Point out each leukocyte.
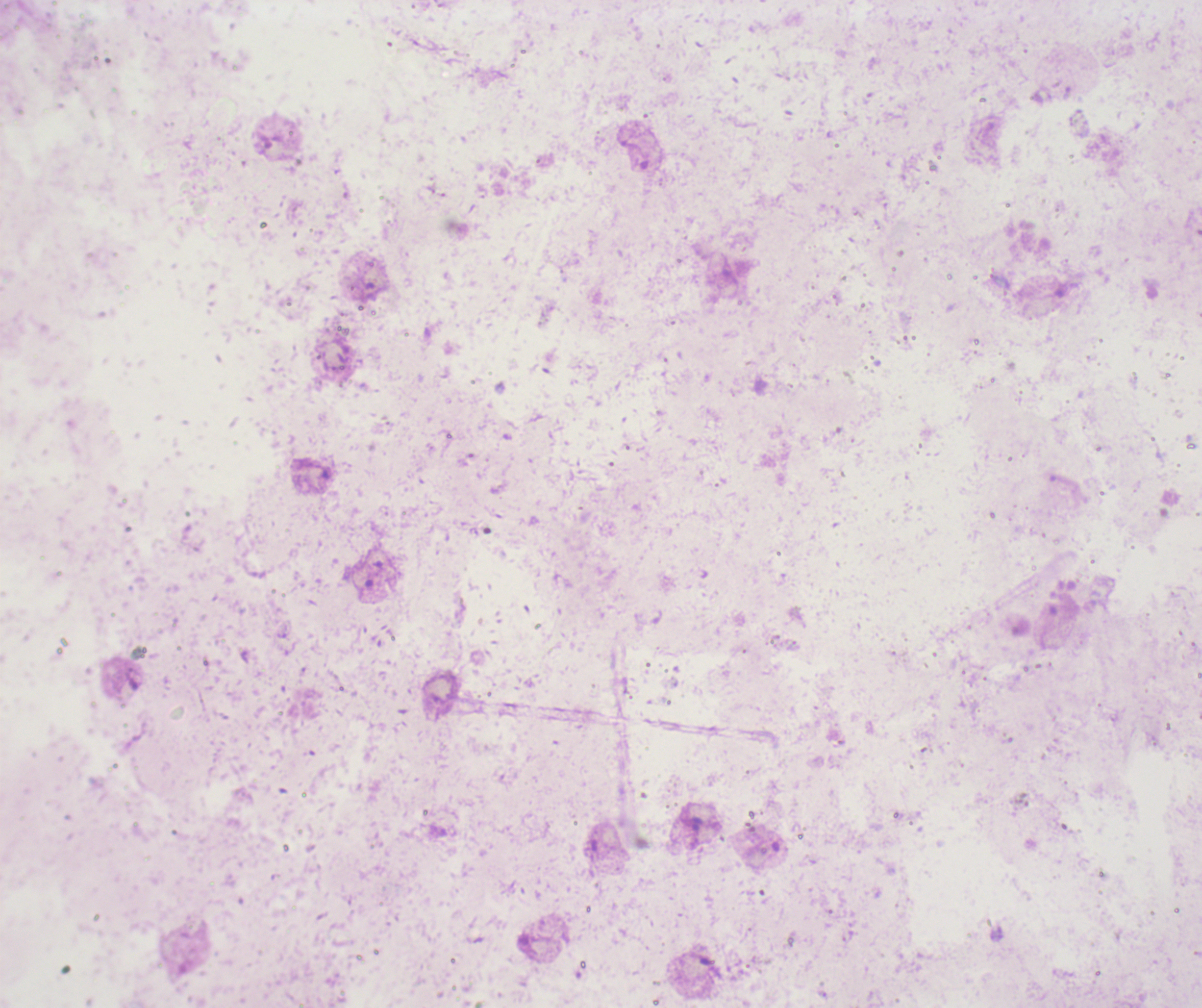
No leukocytes visible.

coordinate format = approximate centers as (x, y) in pixels
trophozoite locations = (697, 823)
preparation = thick blood film
coloration quality = bad
magnification = 100x
field of view = single
background quality = unsatisfactory
context = previously used in a real diagnosis
image size = 1202×1008 pixels
stain = Romanowsky
result = malaria parasites identified